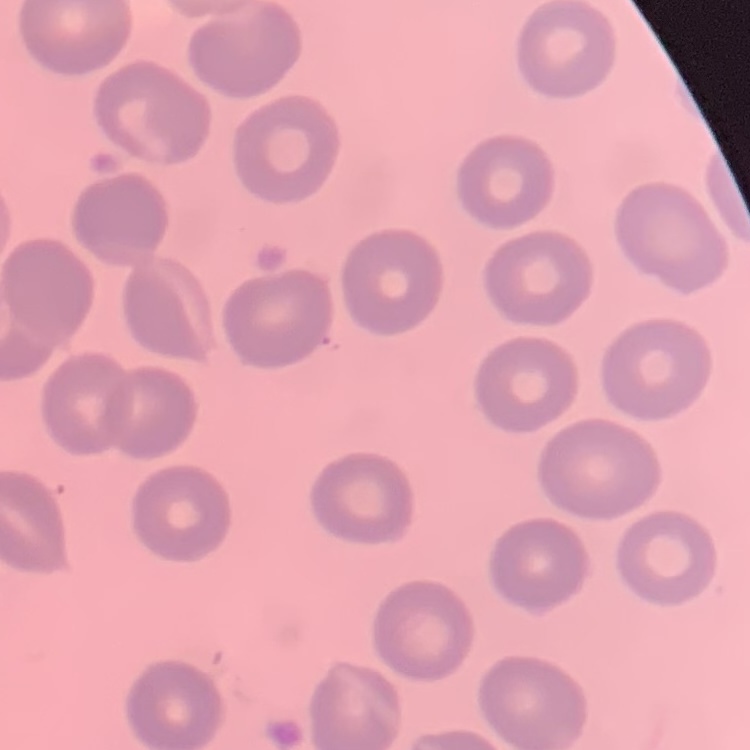
Summary:
  - Red blood cell morphology: no rouleaux formation
  - Image type: one tile cut from a larger photomicrograph
  - Stain: Field's or Giemsa
  - Preparation: thin blood smear